Outline each blood parasite and name the species.
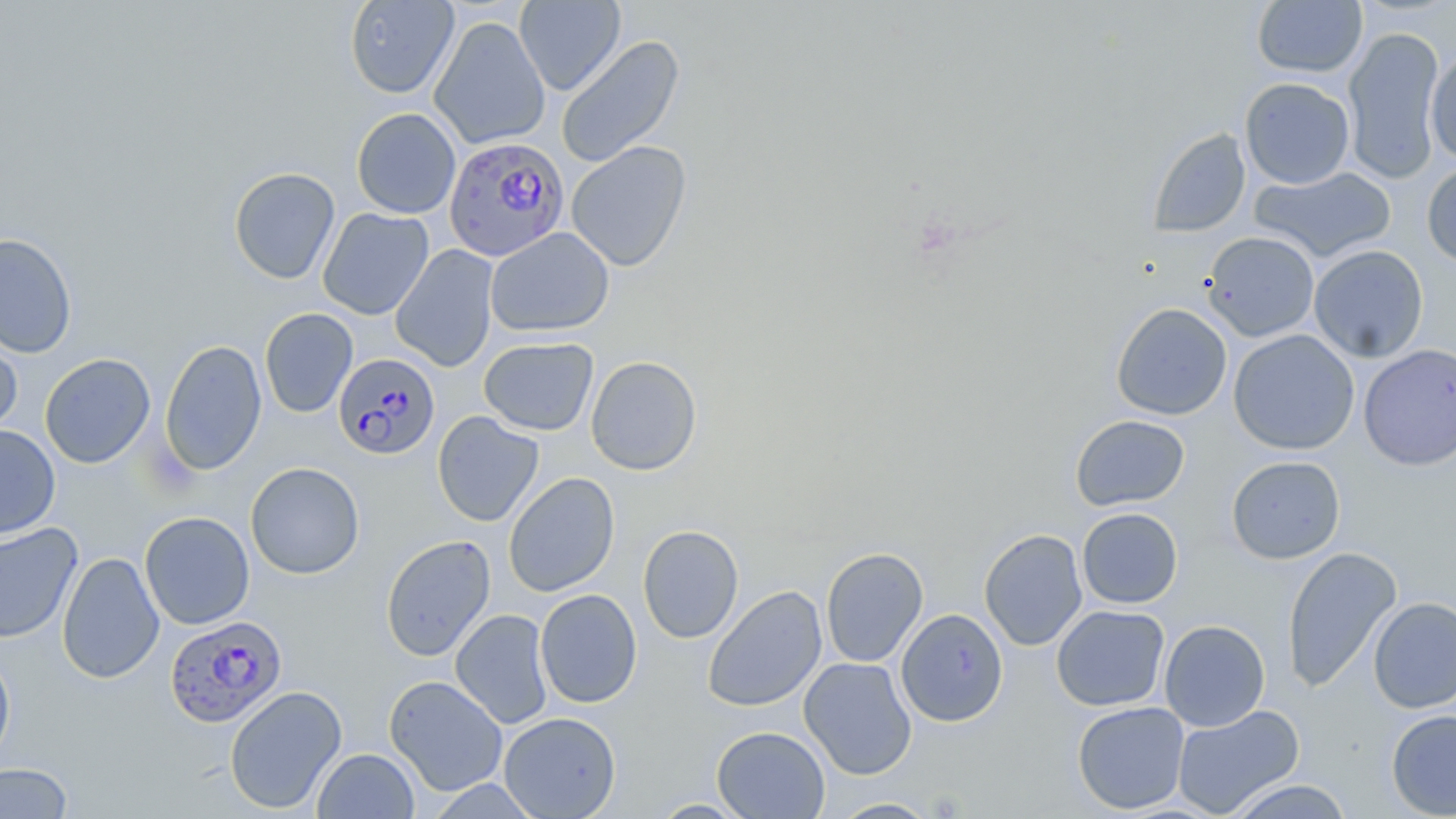

Approximate bounding boxes as (x1, y1, x2, y2) in pixels.
Plasmodium falciparum-infected red blood cells: (443, 137, 566, 261), (334, 352, 441, 460), (164, 615, 287, 728).
No Plasmodium ovale, Plasmodium malariae, Plasmodium vivax, Babesia divergens, or Trypanosoma brucei observed.

slide-level diagnosis = Plasmodium falciparum
field of view = one of a larger specimen
modality = optical microscopy
magnification = 1000x
preparation = thin blood smear
uninfected red blood cell locations = approximate bounding boxes as (x1, y1, x2, y2) in pixels: (344, 0, 459, 99), (514, 0, 625, 95), (1251, 1, 1368, 78), (429, 16, 551, 150), (1342, 27, 1445, 184), (556, 35, 685, 169), (1425, 49, 1456, 162), (1239, 78, 1355, 189), (351, 107, 461, 219), (1147, 128, 1251, 238), (566, 141, 692, 272), (1422, 160, 1456, 269), (1249, 166, 1397, 263), (229, 167, 340, 284), (317, 207, 434, 320), (485, 227, 615, 338), (1202, 231, 1319, 342), (0, 232, 77, 358), (390, 244, 499, 372), (1308, 245, 1429, 363), (1110, 302, 1232, 420), (260, 308, 358, 417), (0, 328, 22, 439), (1228, 329, 1359, 455), (479, 337, 598, 435), (159, 339, 267, 476), (1358, 343, 1456, 471), (39, 353, 155, 469), (586, 355, 702, 476), (432, 411, 544, 527), (1070, 414, 1190, 511), (0, 425, 60, 539), (1226, 455, 1346, 564), (245, 462, 365, 579), (503, 472, 620, 597), (1077, 507, 1183, 609), (139, 511, 255, 630), (0, 523, 83, 643), (638, 525, 743, 643), (979, 529, 1088, 651), (380, 534, 496, 661), (1281, 546, 1402, 693), (820, 548, 928, 668), (57, 551, 164, 684), (702, 585, 827, 712), (535, 589, 642, 708), (1368, 596, 1456, 713), (1051, 605, 1170, 711), (896, 608, 1008, 726), (450, 609, 554, 729), (1159, 620, 1270, 731), (0, 649, 15, 768), (799, 657, 917, 779), (384, 675, 508, 796), (224, 685, 347, 814), (1072, 701, 1190, 814), (1172, 705, 1305, 818), (1386, 709, 1456, 818), (498, 711, 621, 818), (712, 726, 830, 819), (312, 748, 419, 818), (0, 762, 73, 818), (1226, 779, 1354, 818), (826, 797, 942, 818), (650, 799, 752, 818)
stain = May-Grünwald-Giemsa
image size = 1456×819 pixels